Name the parasite shown.
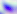

Toxoplasma gondii.

Summary:
  - Modality: micrograph
  - Magnification: 400x